Assess the morphology of the red blood cells.
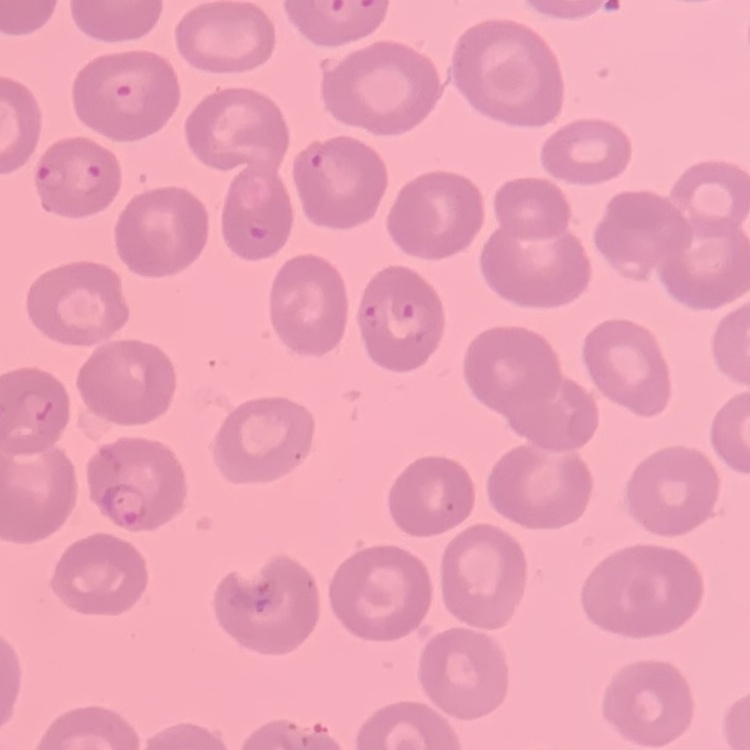
They show no rouleaux formation.

Thin blood film. Field's or Giemsa stain. Square crop of a larger photomicrograph.